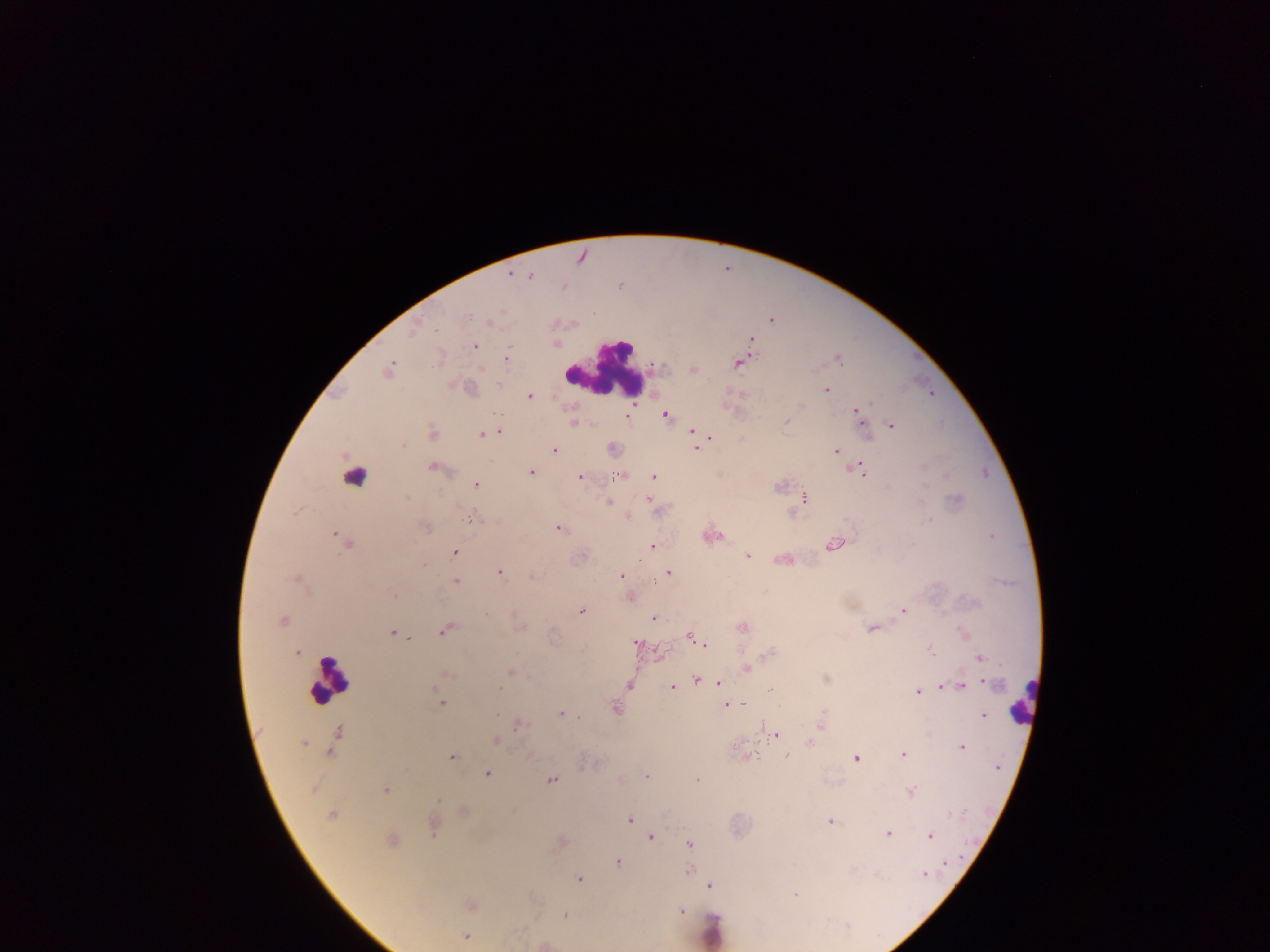
Approximate centers as [x, y] in pixels. Malaria parasite locations: [511, 275], [530, 275], [772, 319], [488, 322], [412, 329], [751, 338], [473, 345], [837, 358], [506, 359], [737, 363], [388, 369], [693, 370], [498, 384], [826, 390], [529, 396], [801, 405], [855, 410], [627, 415], [665, 415], [860, 415], [786, 422], [574, 423], [891, 424], [864, 427], [692, 430], [499, 432], [432, 433], [481, 434], [709, 437], [741, 439], [693, 440], [696, 448], [554, 449], [612, 449], [836, 450], [432, 466], [858, 469], [530, 472], [619, 474], [719, 474], [653, 476], [580, 477], [476, 485], [804, 498], [648, 500], [608, 501], [628, 516], [472, 518], [424, 527], [559, 527], [711, 534], [341, 539], [834, 544], [652, 546], [453, 552], [748, 555], [784, 559], [499, 572], [668, 572], [621, 575], [531, 576], [297, 579], [455, 581], [394, 596], [630, 597], [581, 610], [903, 610], [487, 613], [653, 618], [282, 620], [520, 626], [742, 627], [872, 628], [444, 629], [392, 633], [689, 636], [699, 641], [635, 644], [704, 645], [930, 649], [297, 652], [771, 653], [981, 658], [746, 669], [510, 672], [445, 673], [697, 678], [825, 678], [986, 681], [718, 683], [629, 684], [941, 685], [962, 686], [672, 687], [916, 691], [768, 692], [439, 701], [725, 704], [614, 707], [561, 713], [983, 715], [821, 722], [519, 724], [775, 734], [335, 738], [495, 740], [810, 742], [303, 743], [962, 747], [530, 755], [786, 755], [902, 755], [451, 756], [748, 756], [855, 758], [997, 767], [486, 773], [646, 776], [552, 779], [696, 781], [311, 788], [385, 790], [910, 792], [464, 812], [331, 815], [629, 820], [829, 821], [432, 825], [887, 834], [928, 836], [650, 837], [391, 841], [560, 843], [689, 843], [617, 862], [945, 862], [688, 870], [925, 874], [876, 875], [578, 879], [710, 885], [795, 893], [470, 905], [681, 911], [565, 914], [466, 937], [543, 944]. Leukocyte locations: [604, 370], [353, 479], [328, 680], [1022, 702], [712, 930]. One field of view. Collected in Ghana. Photographed through a microscope with a mobile-phone camera. Thick blood smear. Image is 1270×952 pixels.